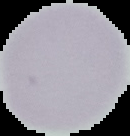

image_size: 130×136 pixels
preparation: thin blood film
image_type: cell region segmented out of the field of view; surrounding area masked to black
result: no Plasmodium parasites seen